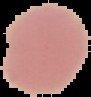
Summary:
  - Preparation: thin blood film
  - Malaria status: uninfected
  - Image size: 91×97 pixels
  - Image type: segmented cell region with the area outside set to black